Locate every Plasmodium parasite.
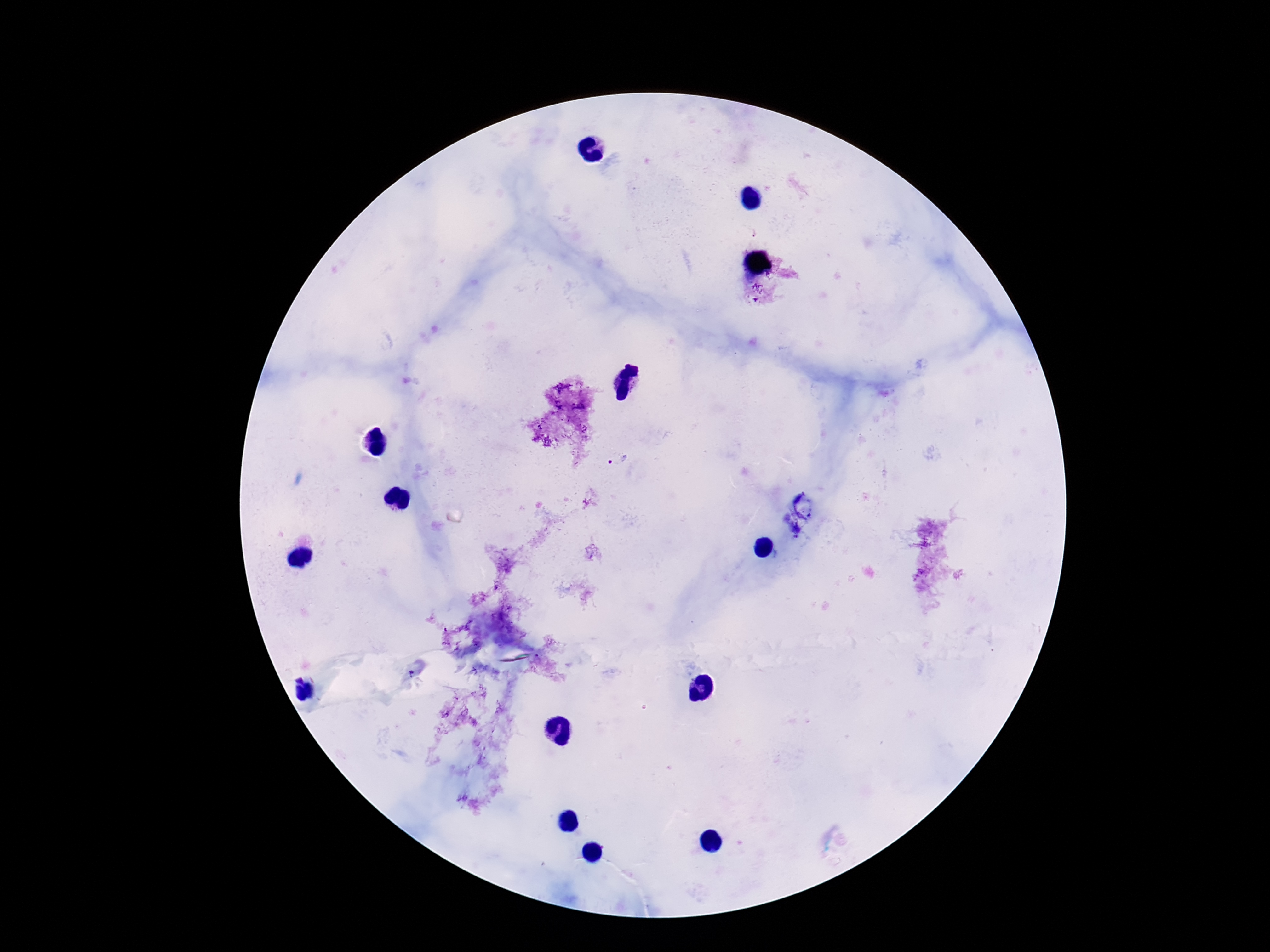
Approximate centers as [x, y] in pixels.
Plasmodium parasites: [619, 462].

100x magnification. Single field of view. Patient malaria status: positive. Image is 1270×952 pixels. Thick blood smear. Photographed through the microscope eyepiece with a smartphone camera. Giemsa stain.